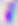
400x magnification. Micrograph. Toxoplasma gondii is seen.